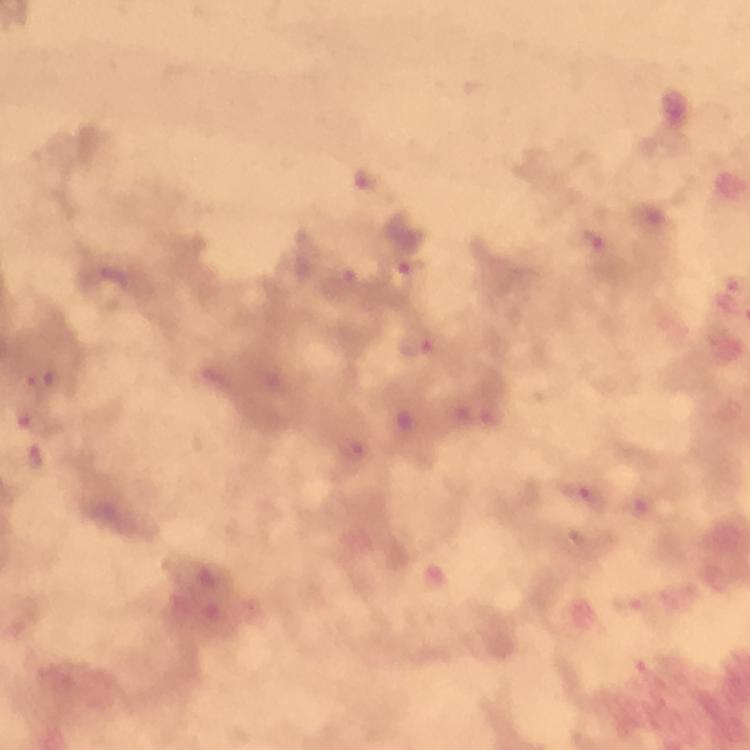 Approximate centers as (x, y) in pixels. Plasmodium parasite locations: (590, 246), (409, 272), (420, 341), (37, 380), (354, 448), (33, 458), (582, 494), (638, 506). Giemsa stain. 100x magnification. Image is 750×750 pixels. From a malaria diagnostic workup. Smartphone photograph taken through a microscope. A crop from one field of view. Immersion oil was used. Thick smear.